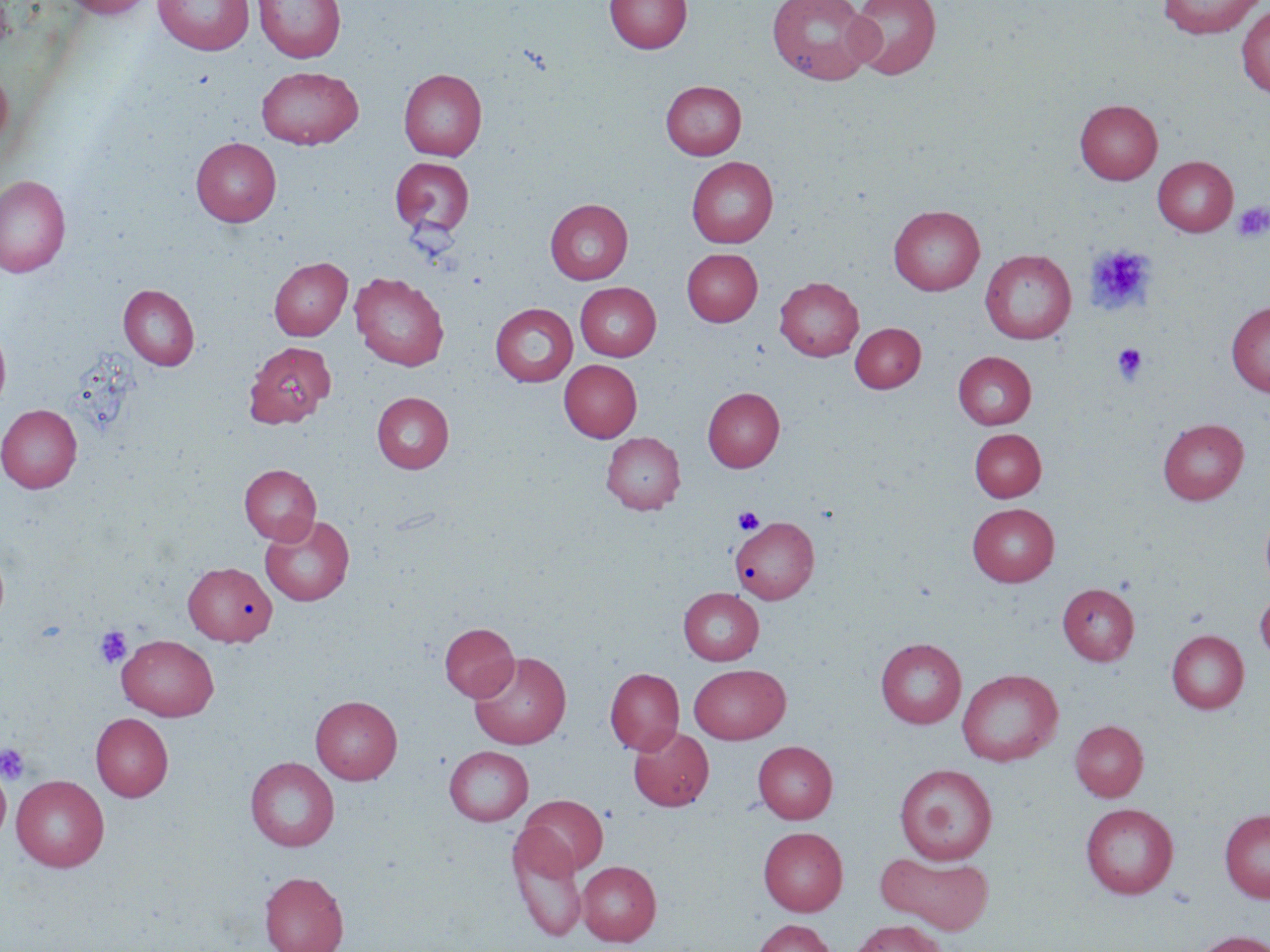

{
  "slide_level_diagnosis": "negative for blood parasites",
  "magnification": "1000x",
  "stain": "May-Grünwald-Giemsa",
  "field_of_view": "single",
  "image_size": "1270×952 pixels",
  "modality": "optical microscopy",
  "uninfected_red_blood_cell_locations": "approximate bounding boxes as named x1/y1/x2/y2 corners in pixels: (x1=60, y1=0, x2=155, y2=18), (x1=153, y1=0, x2=254, y2=55), (x1=253, y1=0, x2=346, y2=63), (x1=604, y1=0, x2=692, y2=54), (x1=766, y1=0, x2=876, y2=85), (x1=847, y1=0, x2=941, y2=79), (x1=1158, y1=0, x2=1266, y2=38), (x1=1236, y1=5, x2=1270, y2=98), (x1=0, y1=61, x2=13, y2=151), (x1=257, y1=66, x2=363, y2=149), (x1=399, y1=68, x2=487, y2=160), (x1=661, y1=81, x2=746, y2=159), (x1=1075, y1=99, x2=1162, y2=184), (x1=191, y1=137, x2=281, y2=226), (x1=1153, y1=156, x2=1238, y2=236), (x1=391, y1=157, x2=475, y2=237), (x1=687, y1=157, x2=778, y2=247), (x1=0, y1=175, x2=71, y2=277), (x1=545, y1=199, x2=633, y2=284), (x1=889, y1=205, x2=985, y2=295), (x1=682, y1=248, x2=762, y2=326), (x1=980, y1=249, x2=1076, y2=344), (x1=269, y1=256, x2=352, y2=340), (x1=350, y1=272, x2=449, y2=370), (x1=775, y1=276, x2=863, y2=360), (x1=575, y1=282, x2=660, y2=360), (x1=119, y1=284, x2=199, y2=369), (x1=490, y1=302, x2=578, y2=386), (x1=1226, y1=302, x2=1270, y2=397), (x1=850, y1=323, x2=926, y2=392), (x1=0, y1=324, x2=11, y2=413), (x1=244, y1=340, x2=335, y2=428), (x1=953, y1=352, x2=1036, y2=429), (x1=559, y1=359, x2=641, y2=442), (x1=703, y1=387, x2=784, y2=471), (x1=372, y1=392, x2=454, y2=473), (x1=0, y1=404, x2=82, y2=493), (x1=1157, y1=418, x2=1249, y2=505), (x1=970, y1=429, x2=1046, y2=502), (x1=601, y1=431, x2=685, y2=514), (x1=239, y1=464, x2=321, y2=544), (x1=967, y1=503, x2=1059, y2=586), (x1=1260, y1=506, x2=1270, y2=595), (x1=260, y1=514, x2=355, y2=606), (x1=730, y1=516, x2=819, y2=604), (x1=184, y1=562, x2=277, y2=646), (x1=1057, y1=583, x2=1139, y2=665), (x1=678, y1=587, x2=764, y2=665), (x1=1255, y1=589, x2=1270, y2=664), (x1=439, y1=623, x2=518, y2=701), (x1=1167, y1=630, x2=1248, y2=713), (x1=117, y1=635, x2=218, y2=720), (x1=876, y1=638, x2=966, y2=728), (x1=469, y1=651, x2=571, y2=749), (x1=689, y1=664, x2=791, y2=743), (x1=605, y1=668, x2=684, y2=755), (x1=957, y1=668, x2=1063, y2=766), (x1=310, y1=695, x2=402, y2=784), (x1=91, y1=713, x2=173, y2=801), (x1=1070, y1=720, x2=1148, y2=801), (x1=628, y1=726, x2=714, y2=811), (x1=753, y1=741, x2=837, y2=823), (x1=444, y1=745, x2=533, y2=826), (x1=245, y1=757, x2=339, y2=851), (x1=895, y1=763, x2=997, y2=865), (x1=0, y1=764, x2=11, y2=846), (x1=11, y1=775, x2=109, y2=872), (x1=518, y1=795, x2=607, y2=875), (x1=1081, y1=803, x2=1178, y2=898), (x1=1219, y1=809, x2=1270, y2=902), (x1=507, y1=826, x2=588, y2=942), (x1=758, y1=827, x2=848, y2=915), (x1=877, y1=852, x2=995, y2=934), (x1=577, y1=861, x2=661, y2=945), (x1=259, y1=871, x2=349, y2=952), (x1=752, y1=918, x2=835, y2=952), (x1=849, y1=919, x2=949, y2=952), (x1=1189, y1=930, x2=1270, y2=952)",
  "platelet_locations": "approximate bounding boxes as named x1/y1/x2/y2 corners in pixels: (x1=1232, y1=201, x2=1270, y2=242), (x1=1085, y1=244, x2=1155, y2=315), (x1=1112, y1=344, x2=1147, y2=384), (x1=733, y1=507, x2=764, y2=533), (x1=94, y1=626, x2=132, y2=669), (x1=0, y1=742, x2=31, y2=785)",
  "preparation": "thin blood smear"
}